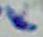 Toxoplasma gondii is shown. 1000x magnification. Micrograph.